State which parasite is depicted.
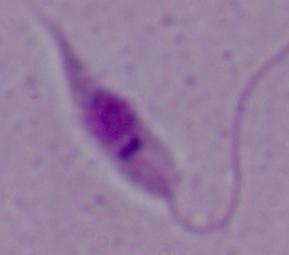
This is Leishmania.

modality: micrograph
magnification: 1000x